Give a bounding box for every malaria parasite, every leukocyte, and every artifact (stain precipitate or debris).
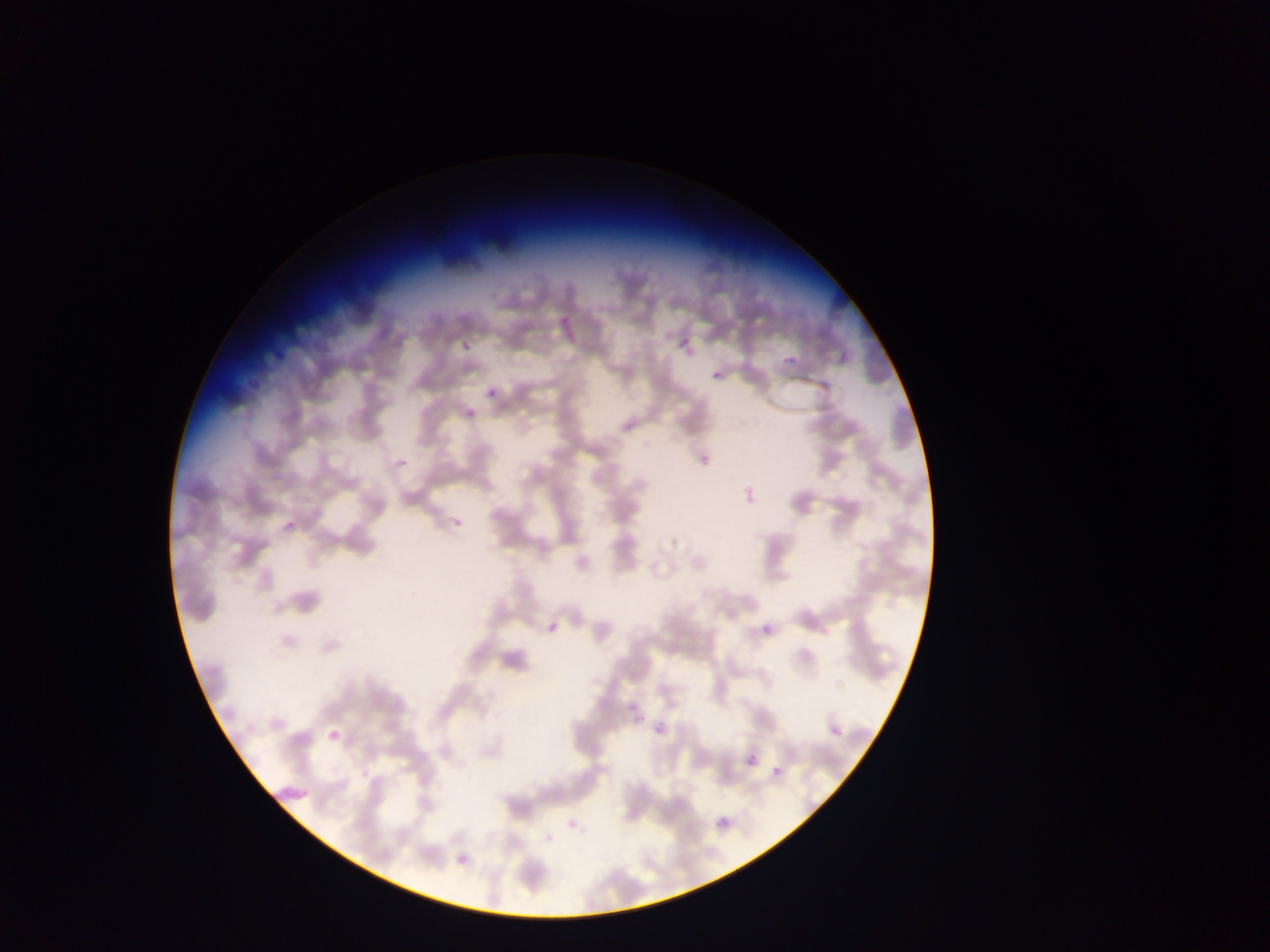
Approximate bounding boxes as {left, top, right, bottom} in pixels.
Malaria parasites: {557, 314, 578, 342}, {678, 339, 690, 348}, {779, 351, 807, 370}, {712, 370, 722, 381}, {487, 390, 498, 398}, {548, 622, 561, 632}, {759, 623, 774, 643}, {629, 712, 645, 732}, {831, 714, 847, 741}, {646, 720, 673, 739}, {323, 724, 342, 745}, {741, 749, 762, 770}, {771, 757, 791, 780}, {273, 783, 314, 801}, {716, 815, 730, 829}.
No leukocytes observed.

Summary:
  - Country: Ghana
  - Preparation: thin blood film
  - Image size: 1270×952 pixels
  - Field of view: single
  - Capture: mobile-phone photograph through a microscope